State which parasite is depicted.
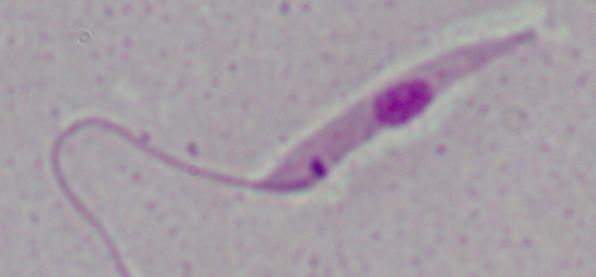
Leishmania.

Summary:
  - Magnification: 1000x
  - Modality: photomicrograph